Outline each blood parasite and name the species.
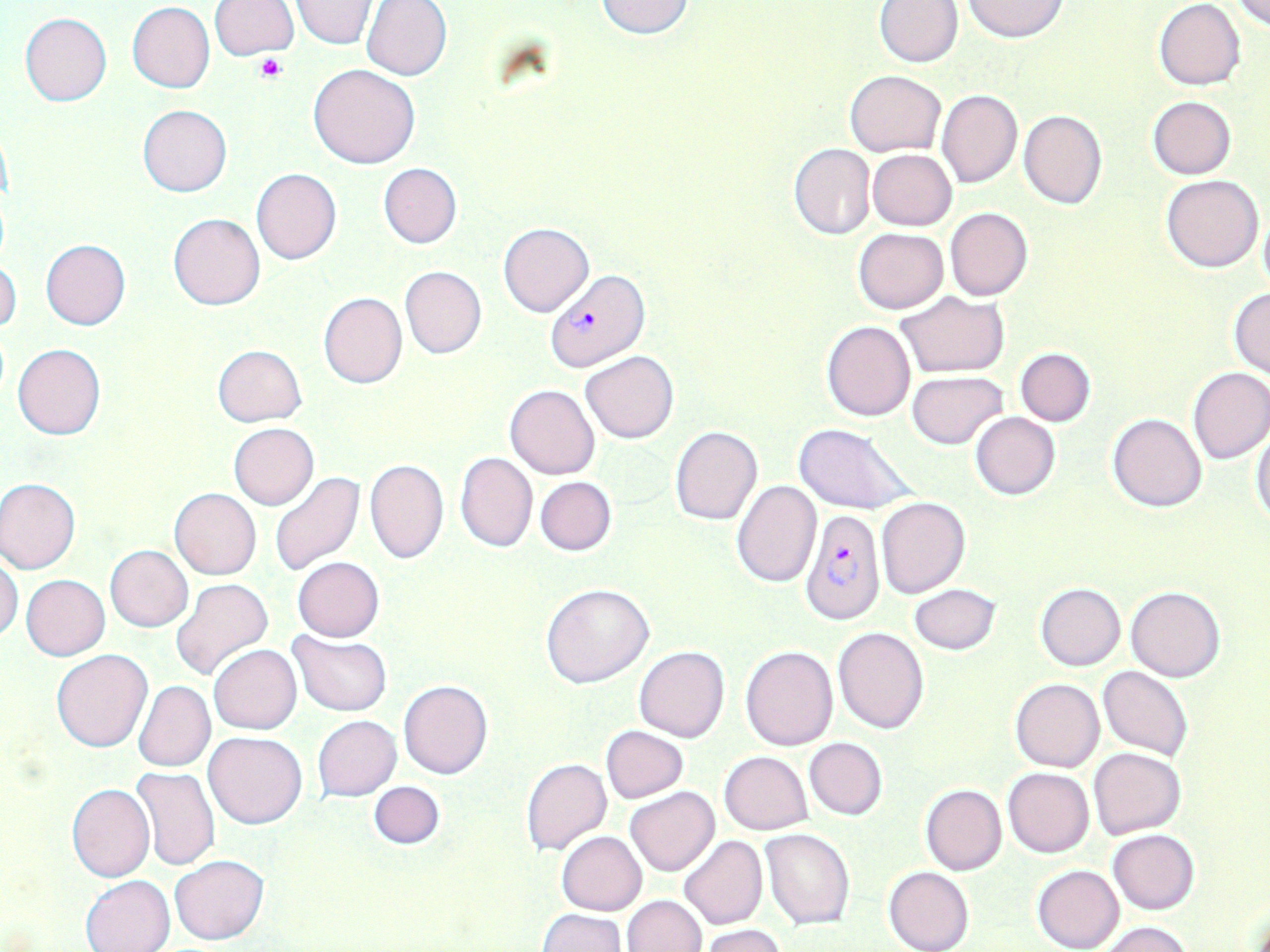
Approximate bounding boxes as [x1, y1, x2, y2] in pixels.
Plasmodium falciparum-infected red blood cells: [544, 270, 650, 374], [803, 509, 886, 624].
No Plasmodium ovale, Plasmodium malariae, Plasmodium vivax, Babesia divergens, or Trypanosoma brucei observed.

Platelet locations: [252, 54, 286, 82]. Uninfected red blood cell locations: [291, 0, 377, 49], [593, 0, 697, 41], [1153, 0, 1245, 91], [1232, 0, 1270, 27], [209, 1, 300, 60], [362, 1, 452, 81], [875, 1, 962, 68], [964, 1, 1066, 41], [127, 2, 215, 92], [20, 13, 112, 106], [308, 63, 420, 169], [847, 71, 946, 155], [936, 89, 1022, 188], [1148, 96, 1237, 180], [138, 104, 231, 197], [1019, 110, 1106, 208], [788, 144, 876, 241], [867, 148, 957, 230], [378, 163, 461, 249], [252, 168, 341, 264], [1162, 174, 1264, 273], [945, 206, 1032, 301], [1259, 210, 1270, 297], [168, 212, 266, 311], [499, 222, 593, 316], [853, 228, 949, 314], [40, 238, 130, 329], [0, 259, 21, 335], [400, 266, 486, 359], [1229, 286, 1270, 377], [896, 292, 1008, 378], [318, 293, 406, 389], [821, 321, 915, 421], [13, 343, 105, 440], [212, 344, 306, 427], [1015, 347, 1096, 425], [581, 351, 679, 443], [1188, 368, 1270, 464], [906, 370, 1008, 449], [504, 384, 600, 479], [971, 413, 1060, 500], [1108, 413, 1207, 512], [228, 423, 319, 509], [793, 423, 917, 515], [669, 426, 762, 526], [1251, 429, 1270, 525], [455, 452, 538, 553], [365, 460, 449, 565], [269, 473, 364, 577], [534, 476, 616, 556], [0, 477, 80, 574], [732, 481, 821, 587], [170, 488, 261, 579], [877, 497, 970, 598], [105, 544, 193, 631], [0, 555, 23, 644], [292, 557, 385, 642], [21, 574, 110, 660], [170, 578, 274, 683], [541, 583, 654, 688], [909, 583, 1001, 656], [1035, 583, 1126, 670], [1125, 586, 1225, 683], [834, 626, 929, 733], [289, 631, 393, 716], [209, 644, 302, 734], [633, 646, 729, 742], [740, 646, 838, 751], [51, 650, 153, 753], [1099, 666, 1192, 761], [1010, 678, 1105, 772], [398, 680, 493, 780], [134, 681, 215, 772], [312, 716, 400, 800], [601, 725, 688, 803], [204, 731, 306, 829], [803, 737, 887, 820], [1089, 747, 1187, 839], [720, 751, 812, 834], [521, 758, 611, 855], [131, 767, 221, 870], [1004, 768, 1094, 858], [369, 781, 445, 848], [66, 783, 155, 882], [920, 784, 1007, 876], [626, 786, 719, 876], [762, 828, 854, 929], [1108, 829, 1200, 914], [557, 832, 646, 914], [680, 836, 767, 930], [169, 855, 269, 945], [1032, 864, 1124, 952], [883, 866, 973, 952], [81, 875, 174, 952], [622, 895, 706, 952], [537, 909, 625, 952], [1098, 921, 1192, 952], [700, 925, 786, 952]. Slide-level diagnosis: Plasmodium falciparum. May-Grünwald-Giemsa stain. Image is 1270×952 pixels. Thin blood film. Light microscopy. 1000x magnification. Single field of view.